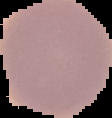
image type = segmented cell region with the area outside set to black
malaria status = uninfected
image size = 112×118 pixels
preparation = thin blood smear